Mark where platelets are.
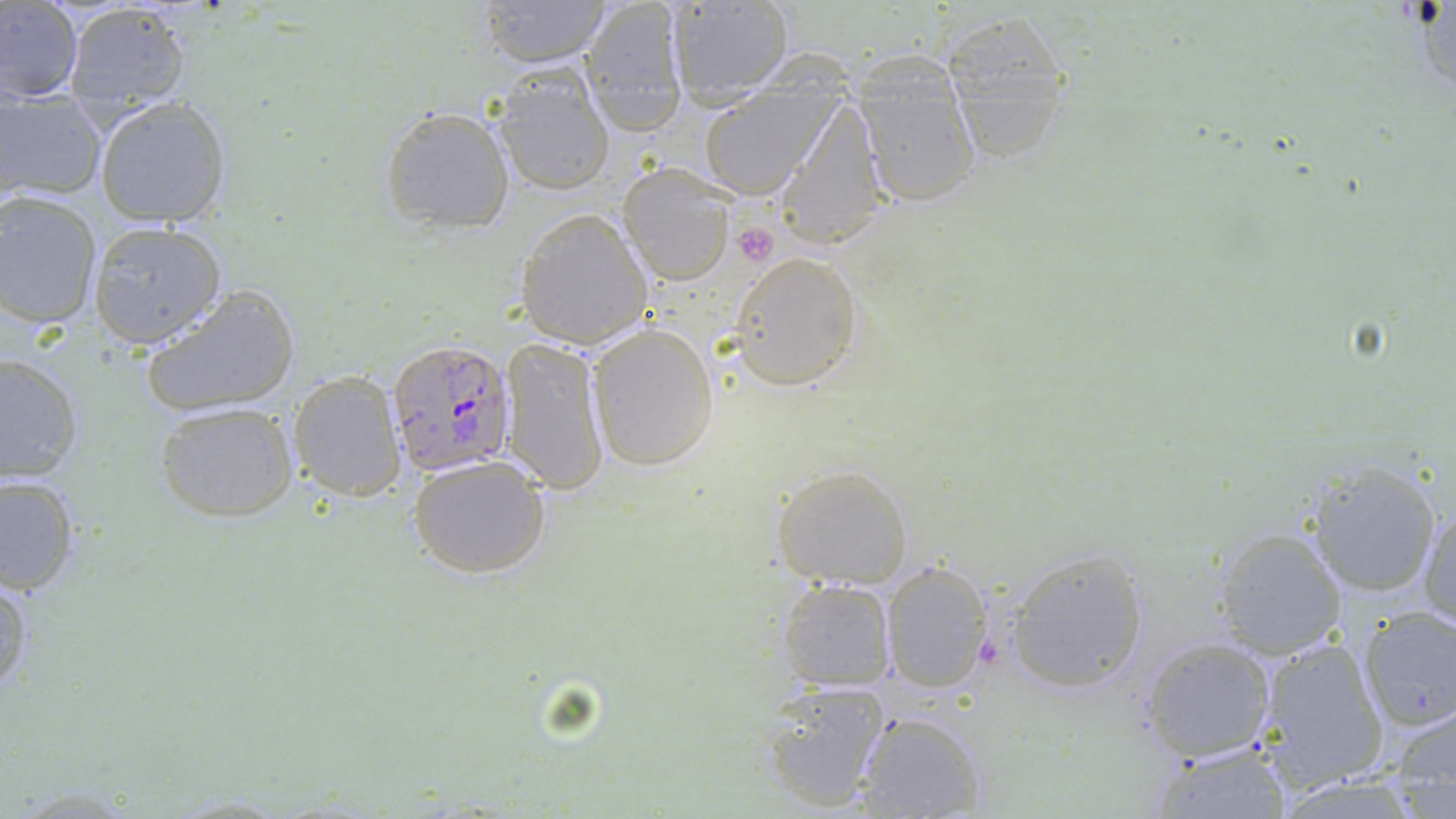
Approximate bounding boxes as [x1, y1, x2, y2] in pixels.
Platelets: [729, 221, 778, 267].

Plasmodium falciparum-infected red blood cell locations: [386, 341, 518, 476]. Uninfected red blood cell locations: [474, 0, 614, 68], [580, 0, 689, 136], [1, 1, 83, 103], [63, 2, 191, 119], [662, 2, 797, 109], [938, 8, 1076, 164], [848, 54, 984, 208], [492, 66, 615, 196], [696, 75, 843, 202], [1, 87, 107, 202], [771, 95, 891, 252], [95, 96, 231, 228], [379, 104, 515, 235], [616, 166, 736, 286], [0, 192, 103, 329], [515, 208, 653, 349], [87, 221, 226, 348], [727, 251, 863, 391], [139, 283, 301, 420], [586, 321, 719, 471], [499, 335, 609, 494], [0, 353, 82, 485], [288, 370, 408, 502], [154, 401, 298, 521], [407, 452, 552, 579], [770, 462, 916, 588], [1302, 463, 1443, 600], [1, 475, 79, 596], [1418, 506, 1456, 630], [1211, 527, 1346, 657], [1002, 547, 1150, 693], [880, 559, 994, 695], [0, 575, 33, 698], [776, 578, 897, 691], [1356, 606, 1456, 731], [1137, 636, 1278, 763], [1254, 637, 1390, 790], [759, 681, 891, 811], [1384, 704, 1456, 817], [852, 710, 986, 819], [1148, 743, 1293, 818]. Slide-level diagnosis: Plasmodium falciparum. Light microscopy. Captured at 1000x magnification. May-Grünwald-Giemsa stain. Thin blood film. One field of a larger specimen. Image is 1456×819 pixels.